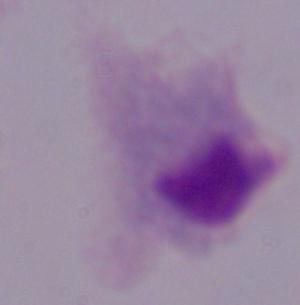
Micrograph. A trichomonad is seen. 1000x magnification.